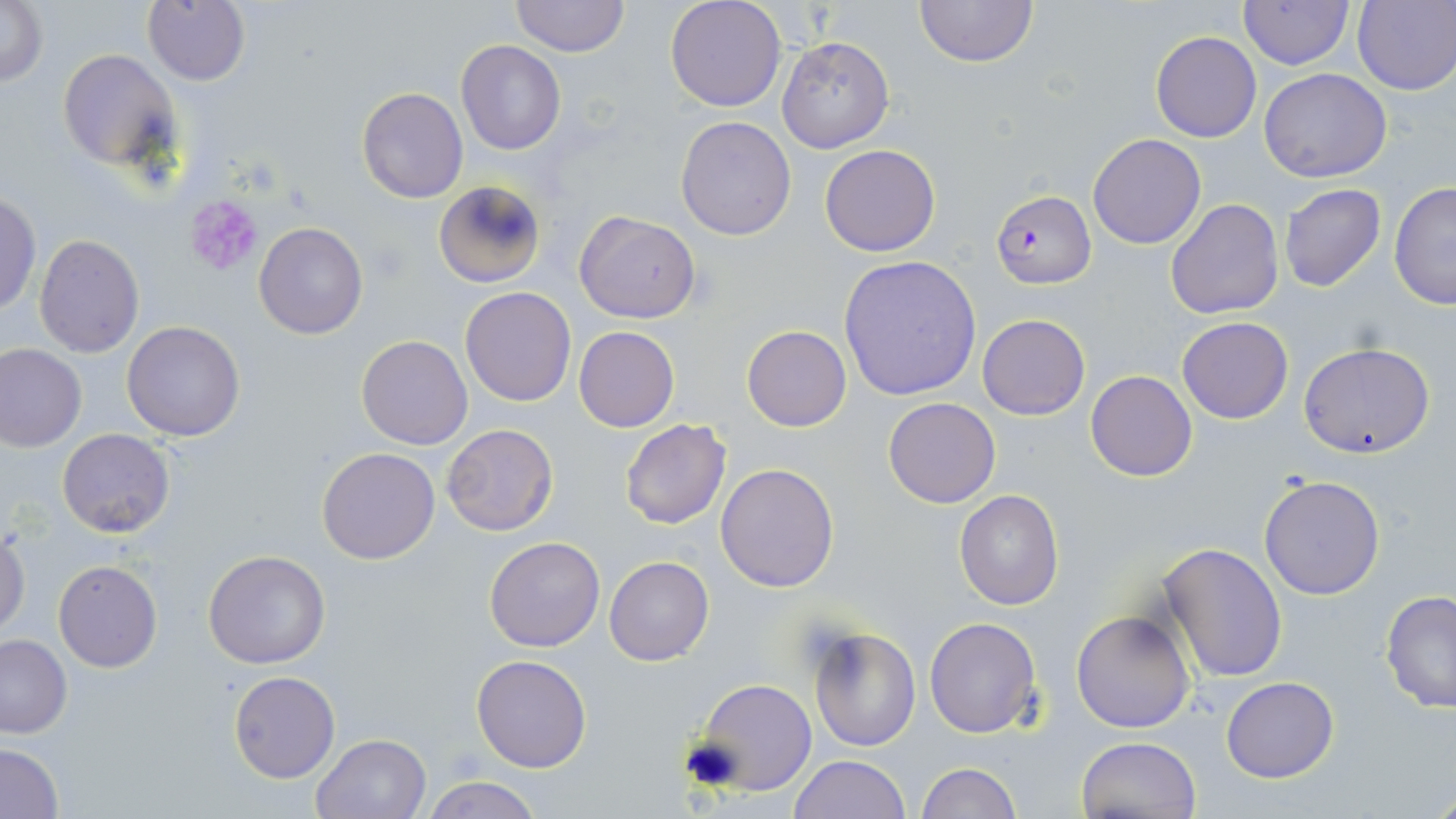

Summary:
  - Coordinate format: approximate bounding boxes as named x1/y1/x2/y2 corners in pixels
  - Platelet locations: (x1=183, y1=195, x2=265, y2=277)
  - Uninfected red blood cell locations: (x1=511, y1=0, x2=628, y2=57), (x1=664, y1=0, x2=787, y2=112), (x1=913, y1=0, x2=1039, y2=68), (x1=2, y1=1, x2=48, y2=87), (x1=1238, y1=1, x2=1354, y2=69), (x1=1353, y1=1, x2=1456, y2=94), (x1=141, y1=2, x2=251, y2=85), (x1=1150, y1=30, x2=1261, y2=142), (x1=775, y1=35, x2=894, y2=154), (x1=455, y1=39, x2=566, y2=155), (x1=57, y1=47, x2=181, y2=171), (x1=1259, y1=68, x2=1391, y2=183), (x1=357, y1=87, x2=468, y2=203), (x1=675, y1=117, x2=796, y2=239), (x1=1088, y1=133, x2=1206, y2=249), (x1=819, y1=143, x2=941, y2=257), (x1=433, y1=179, x2=546, y2=288), (x1=1277, y1=183, x2=1388, y2=294), (x1=1388, y1=183, x2=1455, y2=310), (x1=0, y1=191, x2=41, y2=318), (x1=1165, y1=199, x2=1284, y2=320), (x1=574, y1=210, x2=700, y2=322), (x1=253, y1=221, x2=368, y2=340), (x1=33, y1=236, x2=144, y2=357), (x1=840, y1=256, x2=983, y2=401), (x1=460, y1=287, x2=576, y2=406), (x1=977, y1=314, x2=1089, y2=419), (x1=1176, y1=317, x2=1293, y2=423), (x1=121, y1=320, x2=247, y2=440), (x1=742, y1=325, x2=852, y2=431), (x1=573, y1=326, x2=679, y2=432), (x1=355, y1=335, x2=473, y2=450), (x1=1299, y1=343, x2=1436, y2=459), (x1=0, y1=345, x2=87, y2=452), (x1=1086, y1=370, x2=1197, y2=481), (x1=883, y1=396, x2=1002, y2=509), (x1=619, y1=420, x2=733, y2=531), (x1=441, y1=423, x2=558, y2=537), (x1=58, y1=428, x2=175, y2=539), (x1=317, y1=447, x2=439, y2=565), (x1=716, y1=462, x2=839, y2=593), (x1=1258, y1=474, x2=1386, y2=600), (x1=954, y1=489, x2=1064, y2=611), (x1=0, y1=526, x2=29, y2=638), (x1=483, y1=536, x2=607, y2=653), (x1=1157, y1=542, x2=1288, y2=682), (x1=202, y1=549, x2=331, y2=668), (x1=604, y1=556, x2=714, y2=666), (x1=53, y1=559, x2=163, y2=672), (x1=1379, y1=590, x2=1456, y2=714), (x1=1071, y1=608, x2=1197, y2=734), (x1=924, y1=616, x2=1042, y2=739), (x1=806, y1=626, x2=920, y2=752), (x1=0, y1=633, x2=72, y2=738), (x1=471, y1=654, x2=594, y2=773), (x1=228, y1=670, x2=340, y2=784), (x1=1221, y1=676, x2=1339, y2=783), (x1=694, y1=680, x2=818, y2=796), (x1=311, y1=733, x2=434, y2=819), (x1=1075, y1=736, x2=1202, y2=818), (x1=0, y1=743, x2=64, y2=818), (x1=788, y1=755, x2=911, y2=819), (x1=915, y1=762, x2=1020, y2=819), (x1=421, y1=775, x2=544, y2=819)
  - Plasmodium falciparum-infected red blood cell locations: (x1=992, y1=191, x2=1095, y2=288)
  - Slide-level diagnosis: Plasmodium falciparum
  - Image size: 1456×819 pixels
  - Field of view: single
  - Magnification: 1000x
  - Stain: May-Grünwald-Giemsa
  - Modality: light microscopy
  - Preparation: thin blood film